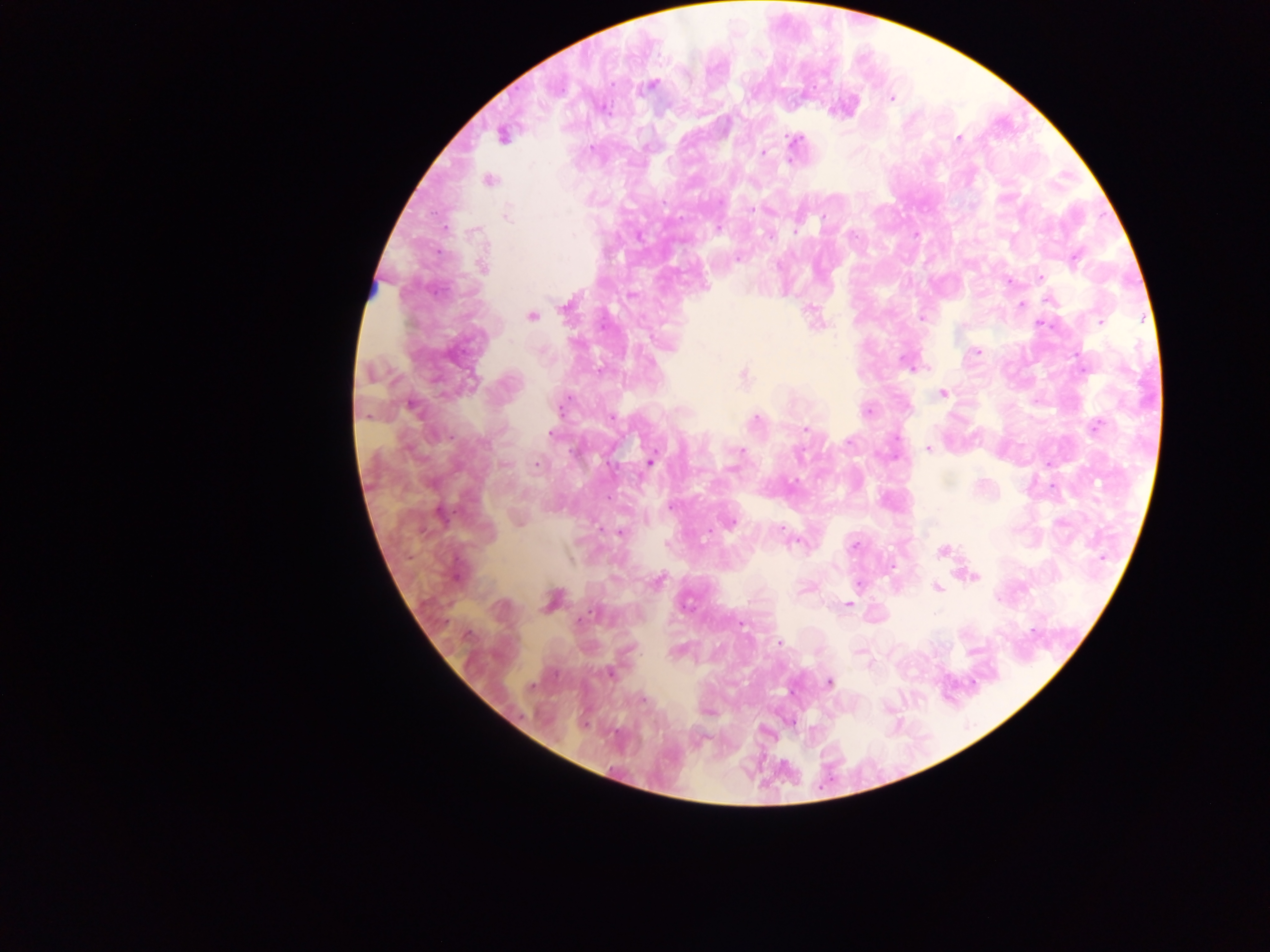

Approximate centers as (x, y) in pixels.
Summary:
  - Plasmodium parasite locations: (652, 85), (891, 98), (606, 110), (502, 136), (959, 139), (795, 140), (764, 152), (791, 158), (489, 180), (752, 210), (506, 216), (823, 219), (718, 228), (797, 229), (1075, 258), (737, 259), (482, 267), (1041, 277), (1049, 300), (1021, 304), (565, 307), (531, 317), (922, 318), (1100, 321), (816, 323), (1043, 325), (978, 352), (904, 360), (743, 375), (471, 381), (943, 394), (412, 407), (868, 411), (755, 421), (1096, 425), (805, 429), (551, 434), (849, 441), (927, 449), (740, 451), (649, 462), (538, 465), (671, 506), (732, 522), (781, 529), (620, 533), (853, 546), (944, 550), (973, 576), (657, 581), (858, 585), (937, 588), (551, 600), (847, 604), (581, 619), (779, 643), (609, 673), (829, 682), (643, 699)
  - Capture: mobile-phone photograph through a microscope
  - Preparation: thick blood smear
  - Field of view: single
  - Country: Ghana
  - Image size: 1270×952 pixels